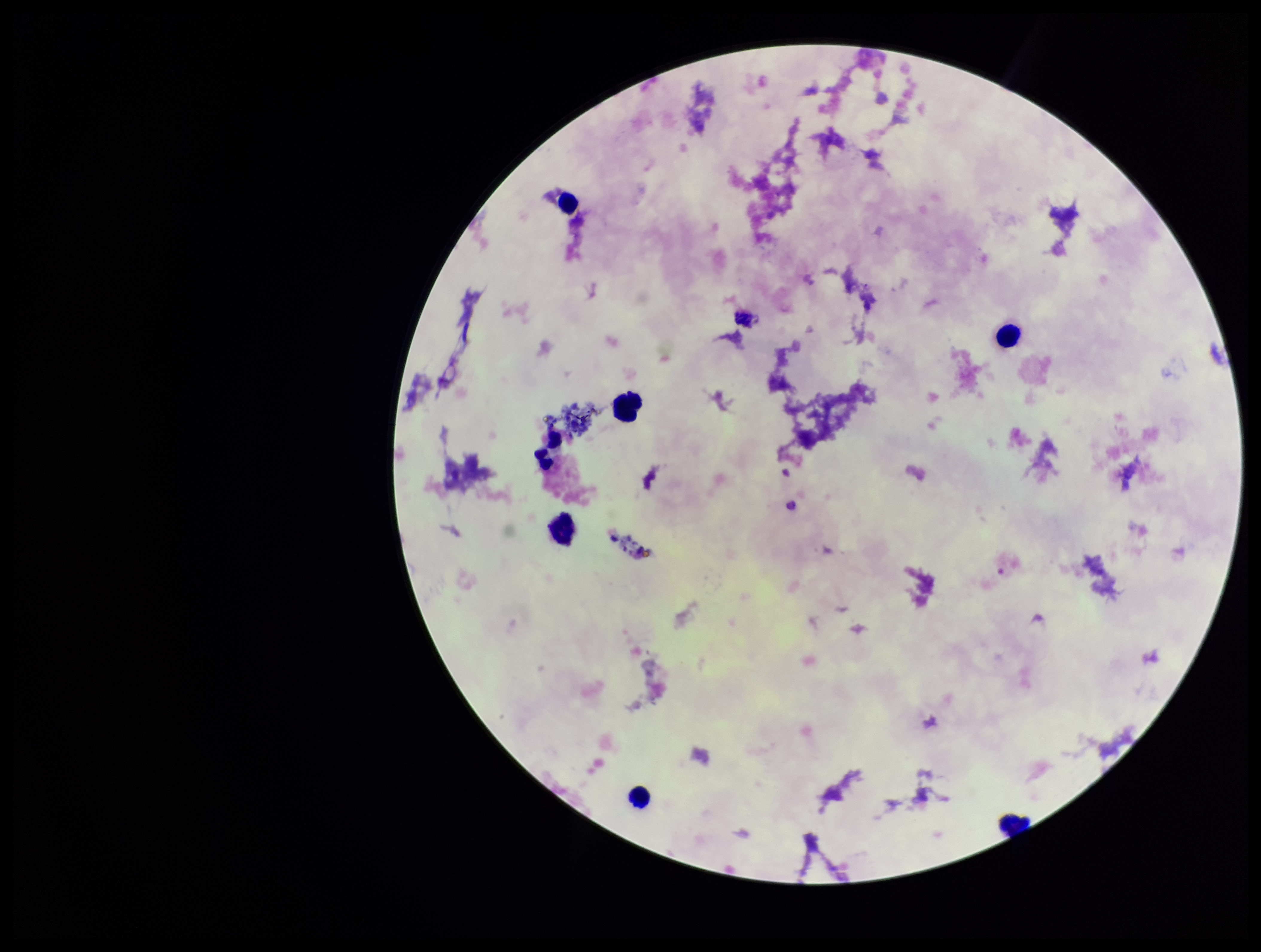
Leukocyte count: 7. Image is 1261×952 pixels. Patient malaria status: negative. Stained with Giemsa. Plasmodium parasites: none identified. Single field of view. Photographed through the microscope eyepiece with a smartphone camera. Parasite count: 0. Preparation: thick.